Describe the morphology of the red blood cells.
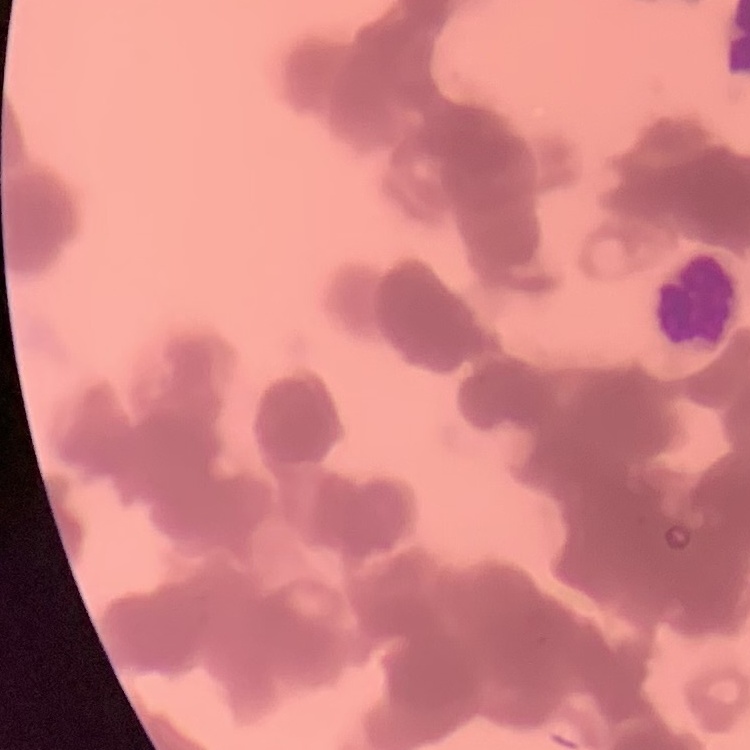

Rouleaux formation.

Summary:
  - Stain: Field's or Giemsa
  - Preparation: thin blood film
  - Image type: one tile cut from a larger photomicrograph